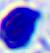

magnification = 400x
identification = leukocyte
modality = micrograph